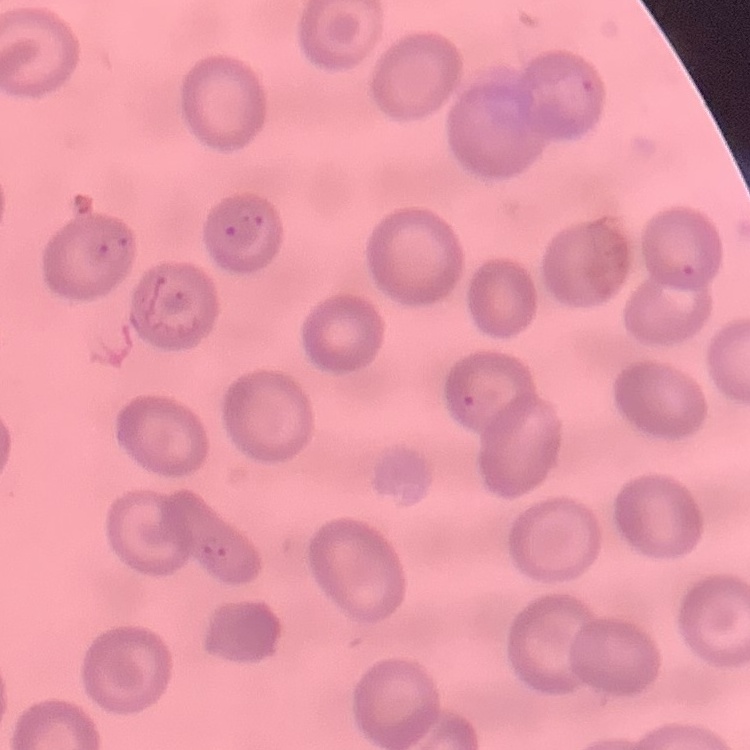

The erythrocytes show no rouleaux formation. Stained with either Field's or Giemsa. One tile cut from a larger photomicrograph. Thin peripheral smear.